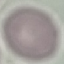 Result: no malaria parasites seen. Acquired by smartphone through the microscope eyepiece. Giemsa stain. Automatically extracted cell patch, resized to 64 × 64 pixels. Thin blood film.